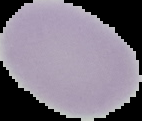
Summary:
  - Image size: 142×121 pixels
  - Image type: segmented cell region on a black background
  - Preparation: thin blood smear
  - Result: no Plasmodium parasites detected